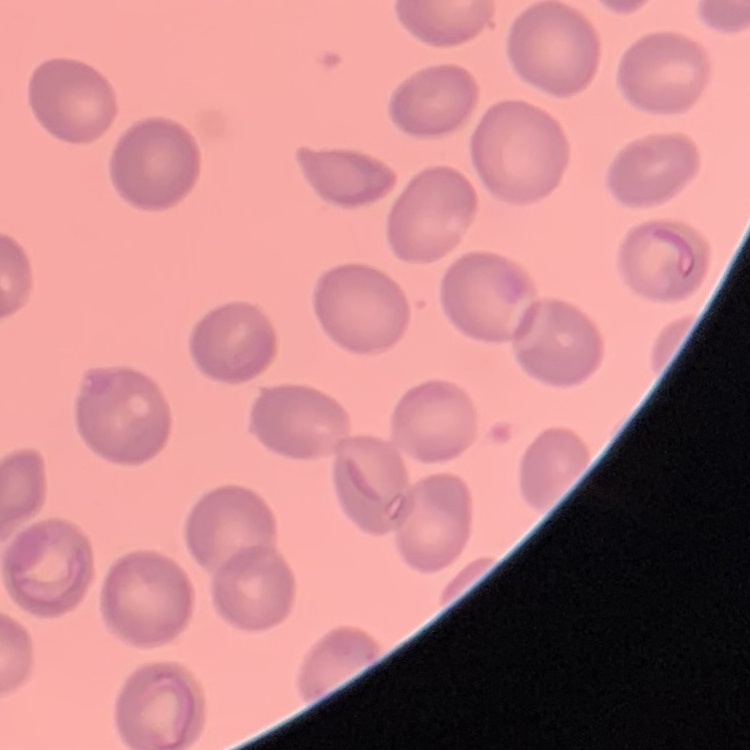
{
  "erythrocyte_morphology": "no rouleaux formation",
  "image_type": "one tile cut from a larger photomicrograph",
  "stain": "Field's or Giemsa",
  "preparation": "thin blood smear"
}